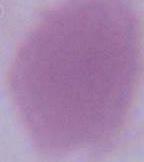

{
  "magnification": "1000x",
  "modality": "micrograph",
  "identification": "red blood cell"
}